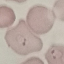 Malaria status: parasitized. Giemsa-stained preparation. Automatically extracted cell patch, resized to 64 × 64 pixels. Photographed with a smartphone camera at the microscope eyepiece. Thin smear of blood.